Report the malaria status of this cell.
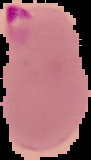

It is parasitized.

Image is 91×160 pixels. Segmented cell region on a black background. From a thin blood film.